Assess this cell for malaria.
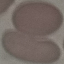

Uninfected.

preparation = thin blood smear
capture = smartphone camera at the microscope eyepiece
stain = Giemsa
image type = cell patch, automatically extracted from a larger field of view and resized to 64 × 64 pixels